Name the parasite shown.
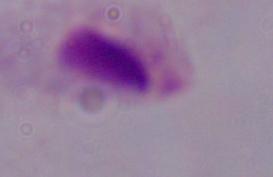
This is a trichomonad.

Summary:
  - Modality: photomicrograph
  - Magnification: 1000x